Describe the morphology of the erythrocytes.
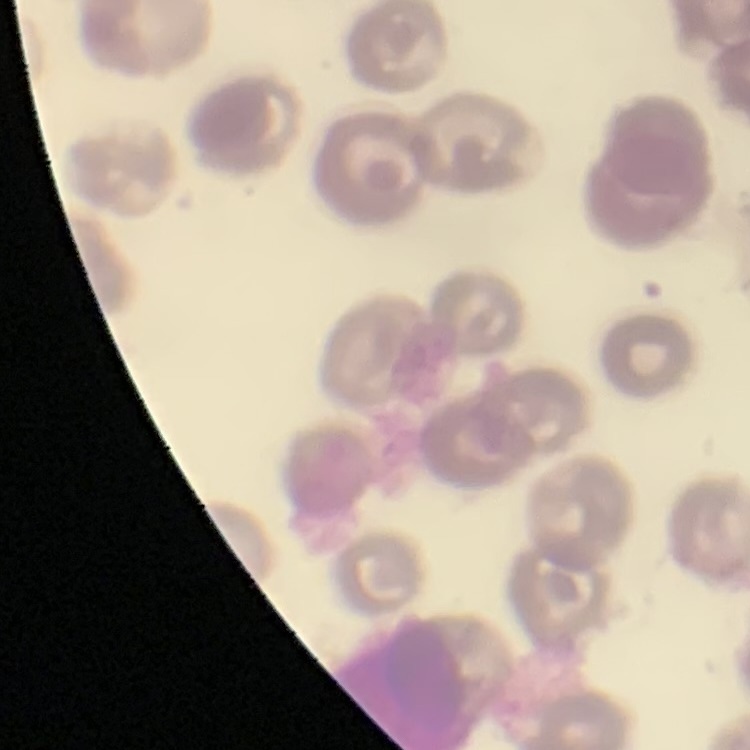

No rouleaux formation.

Summary:
  - Image type: square crop of a larger photomicrograph
  - Preparation: thin blood smear
  - Stain: Field's or Giemsa